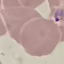

malaria status = parasitized
capture = smartphone through the microscope eyepiece
image type = automatically extracted cell patch, resized to 64 × 64 pixels
stain = Giemsa
preparation = thin blood smear